Assess the morphology of the red blood cells.
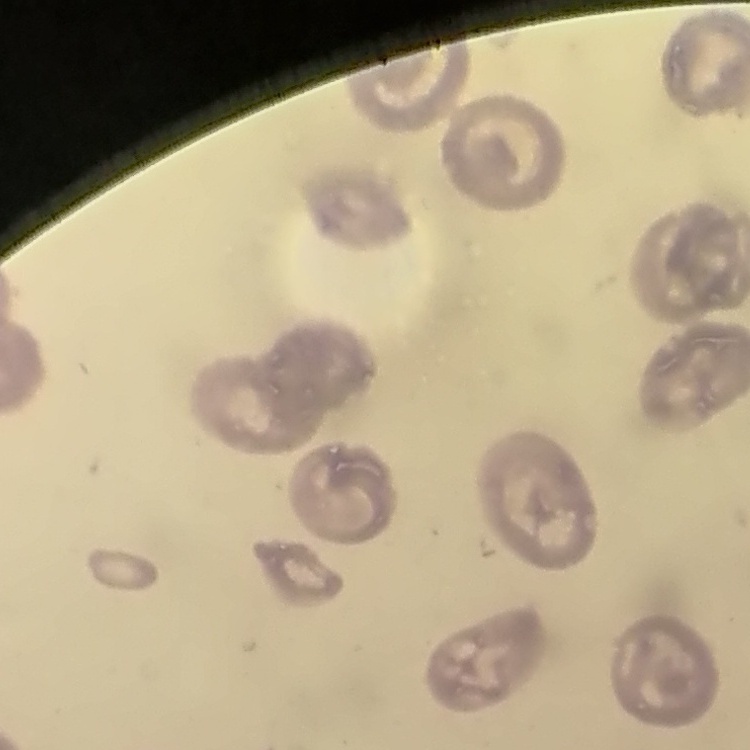

No rouleaux formation.

Thin blood film. Field's or Giemsa stain. One tile cut from a larger photomicrograph.